Identify the preparation type.
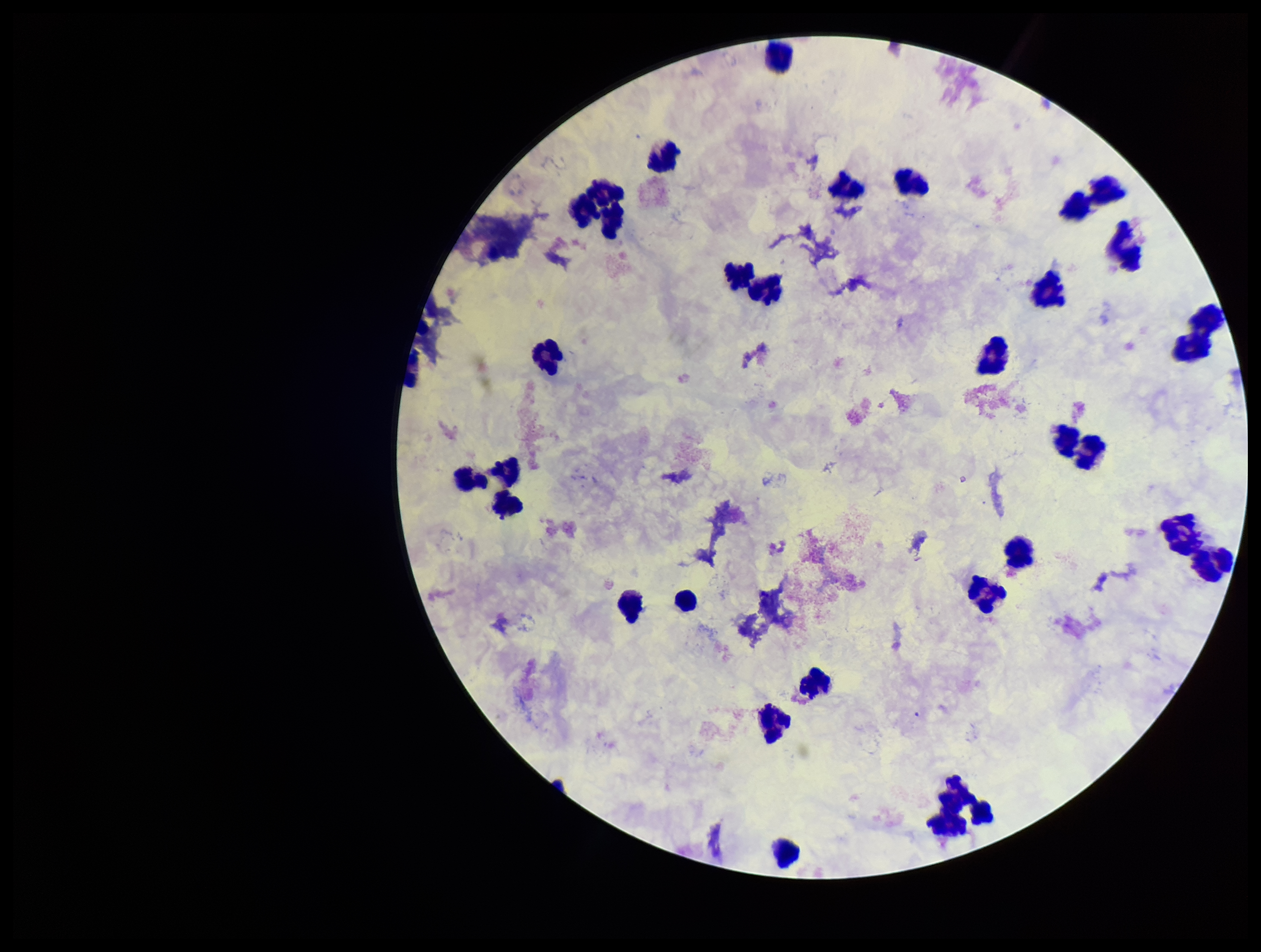

It is a thick blood smear.

Photographed through the microscope eyepiece with a smartphone camera. Leukocyte count: 30. Stained with Giemsa. Parasite count: 0. Image is 1261×952 pixels. Patient malaria status: negative. One field from this slide. Plasmodium parasites: none detected.